Outline each blood parasite and name the species.
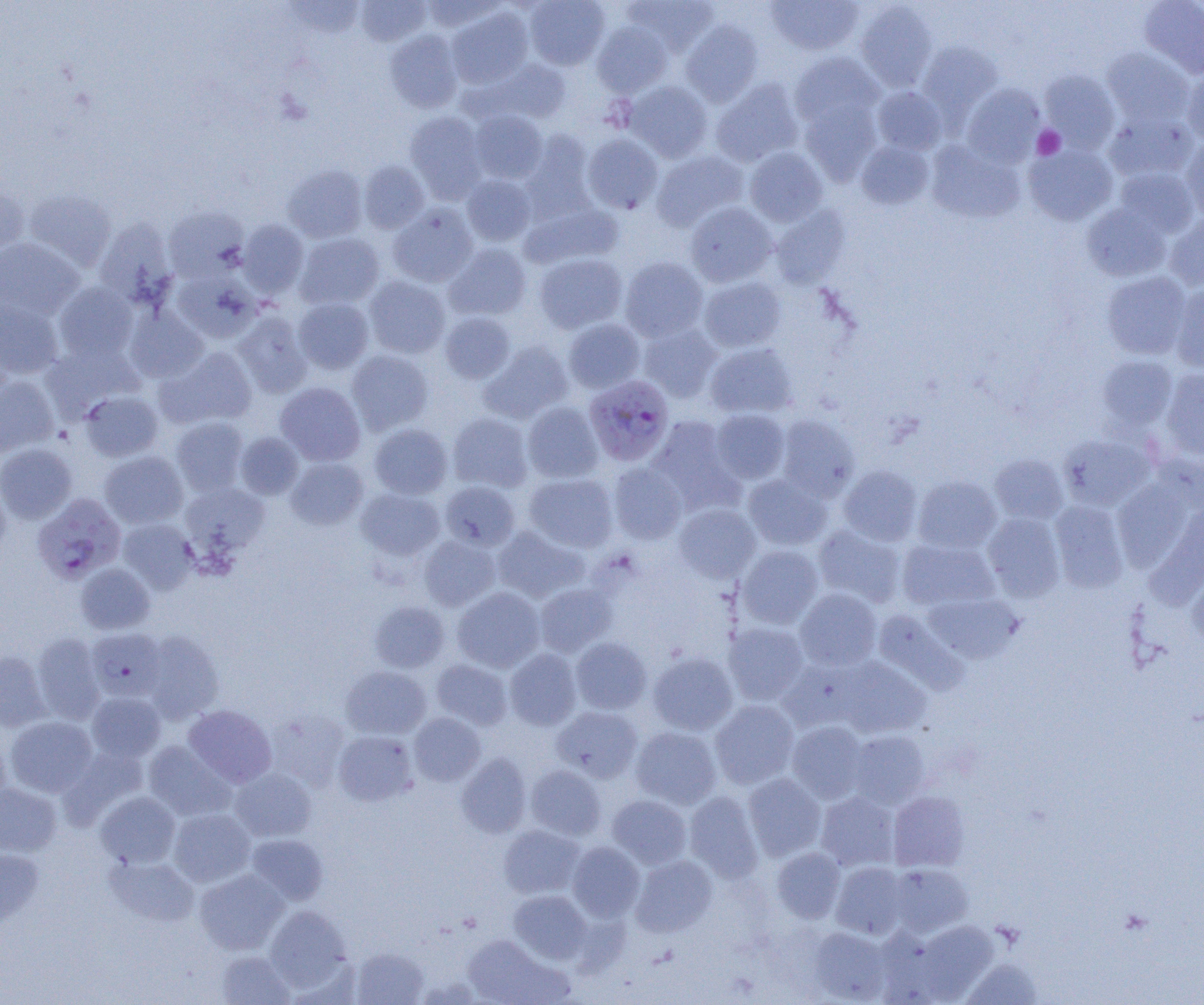
Approximate bounding boxes as (x1,y1)-(x2,y2) corner pairs in pixels.
Plasmodium falciparum-infected red blood cells: (584,375)-(674,466), (33,497)-(128,586), (86,628)-(165,701).
No Plasmodium ovale, Plasmodium malariae, Plasmodium vivax, Babesia divergens, or Trypanosoma brucei observed.

Summary:
  - Uninfected red blood cell locations: (420,0)-(503,32), (525,0)-(610,70), (625,0)-(719,55), (767,0)-(863,55), (1139,0)-(1204,78), (283,1)-(365,39), (356,1)-(430,46), (854,1)-(938,91), (447,6)-(534,88), (681,20)-(763,106), (591,22)-(672,97), (385,30)-(463,113), (917,41)-(1002,120), (1102,47)-(1193,127), (789,52)-(884,129), (486,59)-(571,124), (1040,69)-(1120,152), (1182,71)-(1204,145), (711,78)-(804,167), (624,81)-(712,162), (962,83)-(1045,166), (872,86)-(947,154), (800,98)-(882,184), (469,110)-(547,183), (405,111)-(488,202), (1104,111)-(1198,182), (521,129)-(596,216), (583,134)-(663,213), (926,139)-(1025,224), (1181,139)-(1204,221), (856,140)-(933,209), (1025,143)-(1118,226), (745,147)-(827,226), (651,150)-(748,231), (359,161)-(429,233), (283,165)-(367,243), (1114,167)-(1200,238), (461,175)-(536,246), (0,181)-(28,257), (25,188)-(116,272), (685,201)-(777,287), (521,202)-(623,268), (1082,203)-(1172,282), (388,204)-(478,288), (164,206)-(248,281), (769,206)-(850,288), (1165,213)-(1204,291), (95,218)-(177,306), (239,220)-(308,298), (295,233)-(384,309), (0,237)-(82,321), (444,243)-(531,320), (534,253)-(627,334), (620,256)-(708,342), (173,269)-(260,343), (1102,271)-(1192,359), (364,276)-(450,358), (699,276)-(786,352), (54,282)-(138,363), (1170,285)-(1204,372), (294,297)-(373,374), (0,299)-(63,379), (125,306)-(208,383), (233,311)-(312,398), (440,312)-(515,384), (564,318)-(645,393), (638,322)-(721,402), (479,341)-(573,424), (43,342)-(142,420), (705,343)-(797,419), (158,347)-(258,429), (347,350)-(433,435), (1096,356)-(1177,432), (1161,370)-(1204,457), (0,375)-(58,457), (275,382)-(366,466), (80,391)-(163,461), (523,402)-(603,483), (711,409)-(791,484), (448,413)-(532,492), (777,415)-(859,501), (170,417)-(248,496), (645,417)-(744,515), (369,423)-(452,499), (235,432)-(304,499), (1059,434)-(1153,511), (0,443)-(77,523), (99,451)-(188,529), (990,454)-(1068,524), (286,457)-(368,530), (609,463)-(687,544), (838,465)-(921,545), (524,473)-(618,552), (743,474)-(832,550), (913,476)-(1001,553), (1113,480)-(1192,571), (439,481)-(520,550), (0,482)-(11,563), (182,482)-(269,557), (356,487)-(445,562), (1050,500)-(1128,592), (674,503)-(760,582), (1146,505)-(1204,609), (983,513)-(1065,601), (118,519)-(199,595), (813,524)-(906,608), (492,526)-(587,602), (419,535)-(500,610), (898,538)-(998,611), (737,545)-(823,628), (76,563)-(155,634), (1187,572)-(1204,652), (535,583)-(617,657), (453,587)-(545,672), (795,589)-(881,670), (922,593)-(1022,664), (370,601)-(449,673), (873,609)-(969,695), (724,622)-(809,704), (141,631)-(224,723), (32,633)-(106,724), (571,637)-(652,714), (505,649)-(581,730), (0,650)-(50,731), (649,652)-(738,735), (836,657)-(930,738), (431,659)-(513,730), (341,666)-(431,739), (87,691)-(166,762), (710,700)-(798,789), (184,705)-(276,787), (552,706)-(643,782), (266,710)-(350,791), (409,713)-(485,786), (5,716)-(97,797), (787,721)-(867,803), (631,727)-(721,809), (848,730)-(930,808), (0,731)-(11,812), (334,731)-(417,806), (144,740)-(234,820), (456,753)-(532,838), (526,765)-(606,840), (229,767)-(316,841), (743,773)-(826,861), (0,782)-(61,856), (684,791)-(763,883), (888,791)-(969,871), (96,792)-(180,868), (816,792)-(899,870), (607,795)-(691,868), (168,808)-(255,887), (498,825)-(585,899), (246,834)-(328,905), (567,842)-(644,921), (0,846)-(44,927), (772,848)-(846,923), (106,855)-(199,927), (631,855)-(717,937), (831,863)-(908,939), (888,864)-(973,937), (194,869)-(289,954), (509,890)-(592,964), (265,905)-(351,992), (908,920)-(999,1003), (808,927)-(891,1003), (462,934)-(562,1004), (351,947)-(428,1005), (216,950)-(294,1005), (962,958)-(1042,1004)
  - Platelet locations: (1033,126)-(1065,159)
  - Slide-level diagnosis: Plasmodium falciparum
  - Modality: optical microscopy
  - Preparation: thin blood film
  - Image size: 1204×1005 pixels
  - Field of view: one of a larger specimen
  - Magnification: 1000x